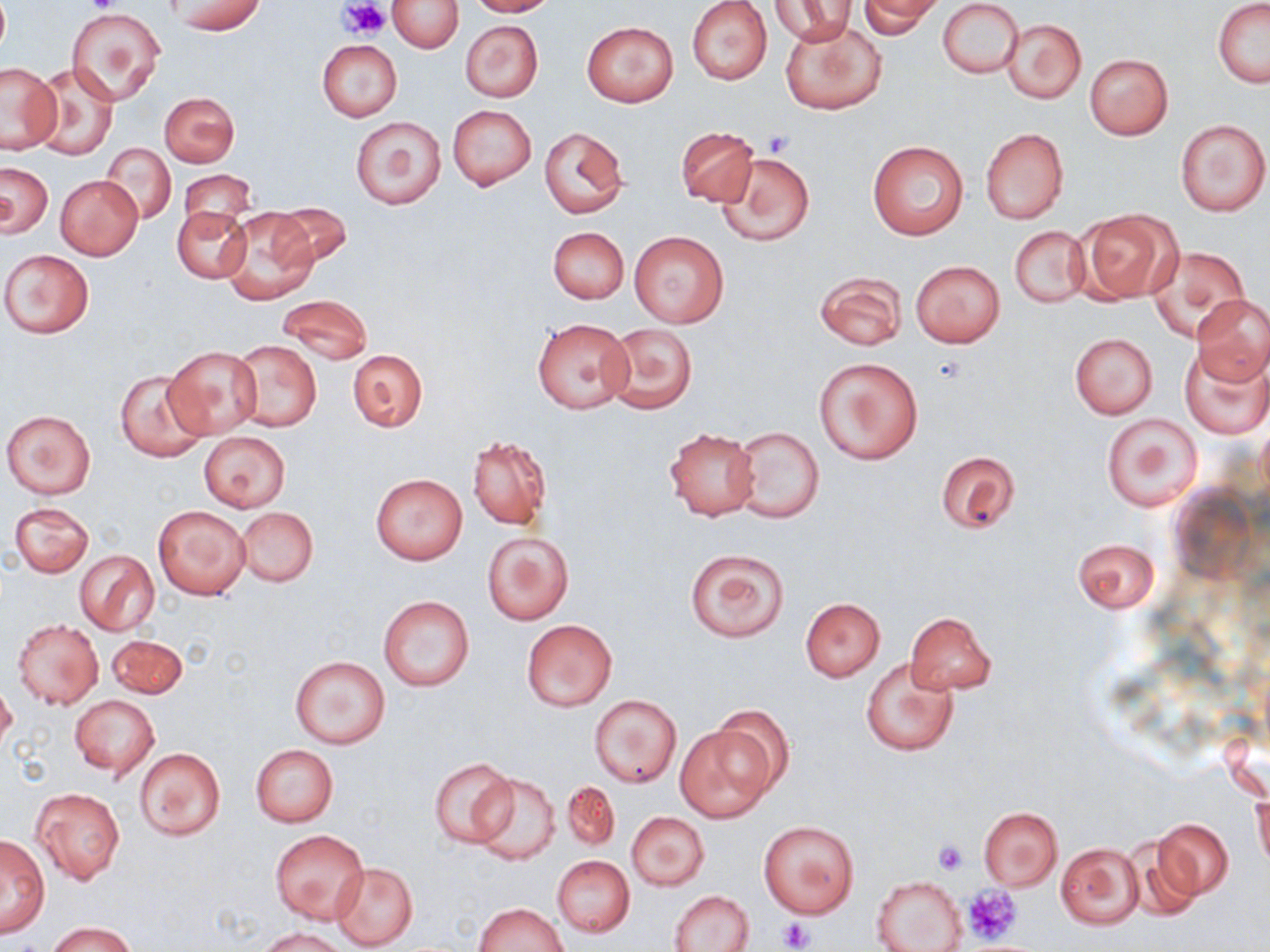
slide_level_diagnosis: negative for blood parasites
modality: optical microscopy
platelet_locations: 'approximate bounding boxes as [x1, y1, x2, y2] in pixels: [84, 0, 116, 15], [339, 0, 390, 39], [763, 130, 794, 157], [933, 839, 968, 874], [963, 884, 1021, 945], [779, 916, 813, 952]'
uninfected_red_blood_cell_locations: 'approximate bounding boxes as [x1, y1, x2, y2] in pixels: [389, 0, 462, 52], [466, 0, 557, 17], [770, 0, 855, 45], [938, 0, 1023, 78], [173, 1, 265, 35], [687, 1, 772, 85], [857, 1, 941, 38], [1213, 1, 1270, 87], [68, 7, 165, 104], [780, 18, 886, 115], [1001, 18, 1086, 103], [459, 19, 544, 102], [582, 21, 678, 106], [317, 40, 402, 122], [1084, 53, 1173, 139], [1, 62, 62, 153], [31, 65, 119, 161], [160, 92, 239, 167], [448, 105, 537, 190], [351, 116, 446, 209], [1174, 117, 1270, 218], [675, 126, 759, 206], [539, 127, 629, 218], [979, 128, 1069, 225], [867, 140, 968, 241], [101, 145, 175, 223], [716, 151, 814, 248], [0, 162, 53, 238], [177, 171, 258, 238], [56, 175, 143, 260], [271, 202, 352, 266], [173, 206, 250, 283], [220, 206, 318, 304], [1076, 208, 1182, 303], [1010, 226, 1090, 308], [547, 227, 629, 303], [630, 231, 728, 328], [1146, 245, 1252, 341], [1, 248, 93, 338], [911, 260, 1004, 348], [815, 270, 907, 351], [1191, 294, 1270, 384], [277, 295, 372, 365], [532, 318, 634, 414], [604, 322, 697, 414], [1068, 333, 1158, 419], [230, 339, 322, 432], [164, 345, 263, 438], [1179, 346, 1270, 438], [347, 349, 428, 432], [816, 357, 922, 463], [114, 369, 211, 462], [2, 409, 98, 499], [1101, 413, 1201, 511], [728, 426, 825, 522], [663, 427, 762, 520], [198, 432, 291, 512], [467, 435, 551, 529], [937, 452, 1021, 534], [370, 473, 468, 564], [9, 501, 94, 577], [153, 504, 250, 600], [235, 507, 318, 587], [482, 531, 574, 626], [1073, 537, 1159, 614], [684, 546, 789, 642], [75, 550, 159, 635], [378, 595, 475, 692], [799, 597, 885, 681], [905, 612, 996, 694], [12, 619, 104, 709], [522, 619, 616, 710], [106, 633, 187, 698], [290, 655, 390, 750], [861, 656, 959, 756], [0, 681, 16, 755], [590, 694, 682, 788], [70, 695, 158, 778], [709, 705, 794, 801], [675, 725, 773, 822], [1219, 727, 1269, 800], [250, 745, 337, 827], [134, 748, 226, 842], [430, 757, 516, 847], [470, 772, 560, 865], [561, 780, 619, 853], [1251, 786, 1269, 868], [32, 787, 124, 886], [977, 807, 1063, 889], [626, 812, 709, 891], [1153, 818, 1234, 900], [759, 820, 859, 918], [270, 829, 368, 924], [1, 833, 49, 937], [1125, 834, 1206, 922], [1055, 842, 1144, 929], [551, 855, 634, 938], [330, 862, 418, 950], [871, 875, 966, 951], [671, 889, 755, 952], [472, 902, 567, 951], [49, 920, 136, 952], [259, 927, 349, 952]'
stain: May-Grünwald-Giemsa
image_size: 1270×952 pixels
preparation: thin blood smear
field_of_view: single
magnification: 1000x